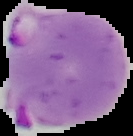 Malaria status: parasitized. From a thin blood smear. Image is 133×136 pixels. The area outside the segmented cell region is set to black.